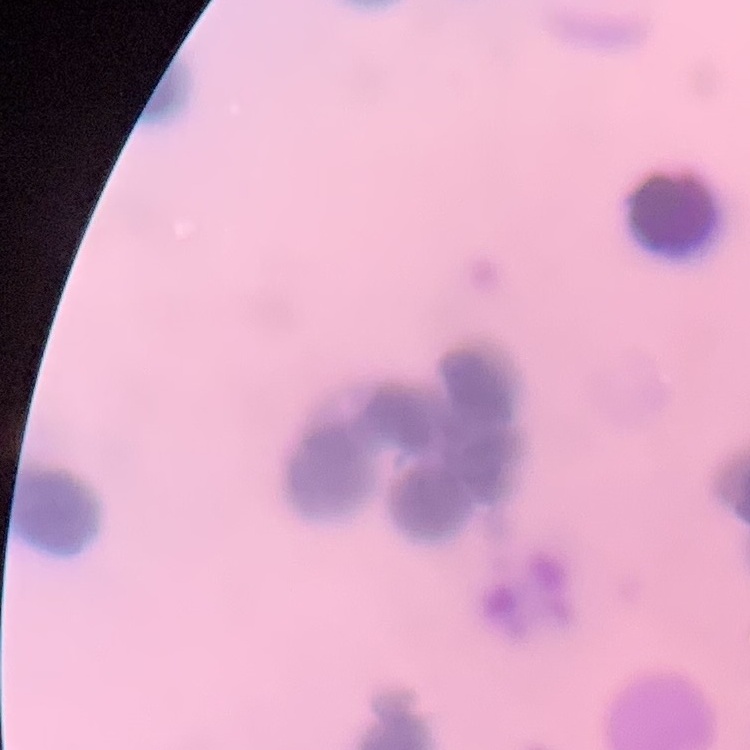 The erythrocytes show rouleaux formation. Square crop of a larger photomicrograph. Stained with either Field's or Giemsa. Thin peripheral smear.